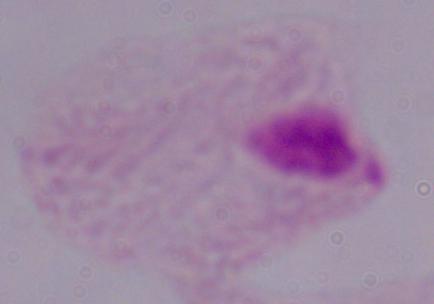

Summary:
  - Identification: trichomonad
  - Magnification: 1000x
  - Modality: micrograph